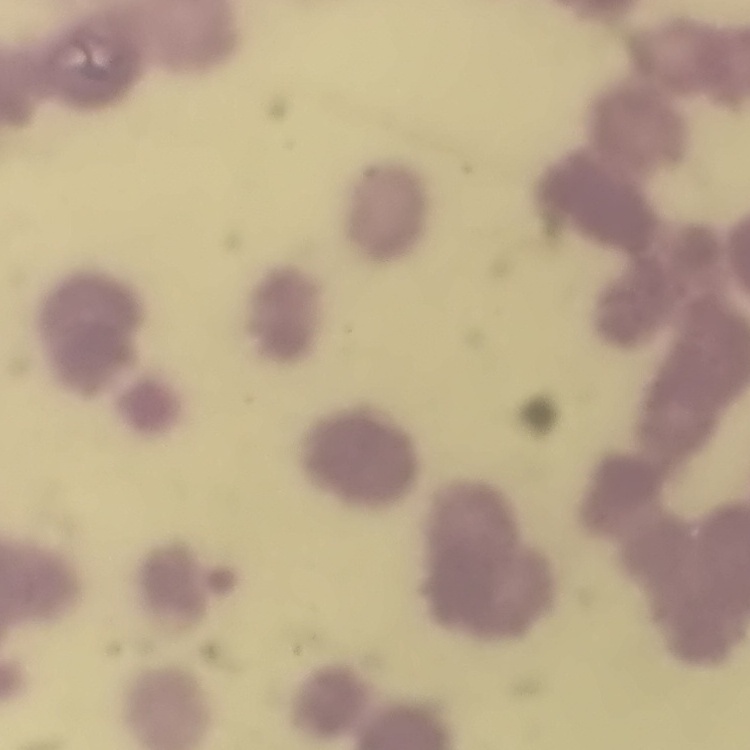
red blood cell morphology = rouleaux formation
preparation = thin blood film
image type = one tile cut from a larger photomicrograph
stain = Field's or Giemsa